Classify this cell by malaria status.
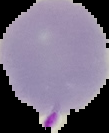

Parasitized.

Image is 109×133 pixels. From a thin blood film. Cell region segmented out of the field of view; the surrounding area is masked to black.